Locate every uninfected red blood cell.
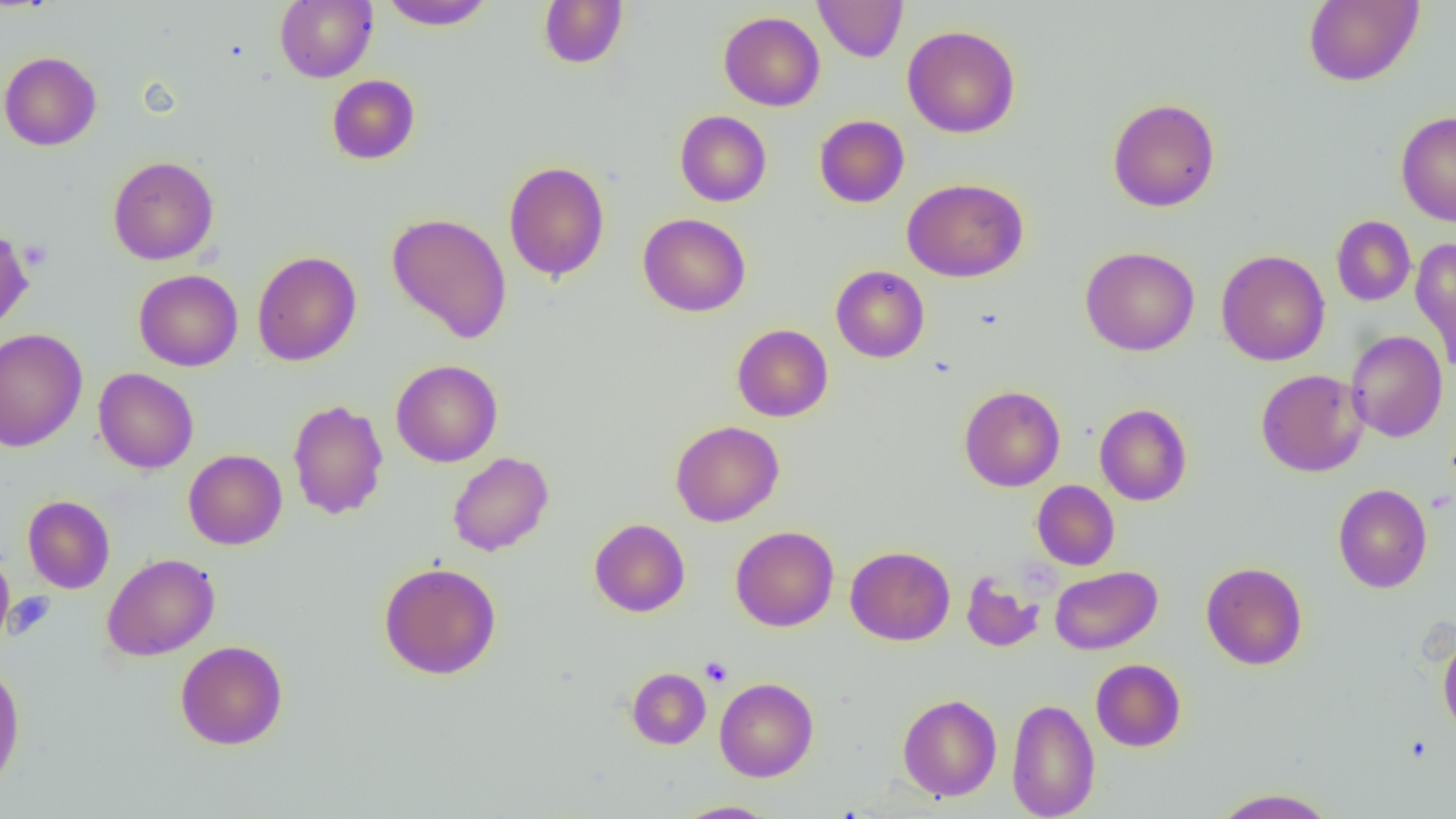

Approximate bounding boxes as [x1, y1, x2, y2] in pixels.
Uninfected red blood cells: [380, 0, 495, 31], [538, 0, 628, 69], [814, 0, 908, 62], [1303, 0, 1424, 87], [275, 1, 378, 82], [718, 11, 825, 111], [902, 25, 1020, 138], [0, 51, 102, 151], [327, 74, 420, 164], [1108, 97, 1220, 212], [675, 110, 772, 207], [1395, 110, 1456, 226], [814, 115, 909, 207], [107, 155, 219, 265], [503, 160, 610, 281], [902, 178, 1028, 282], [387, 212, 512, 344], [638, 213, 751, 317], [1331, 216, 1415, 306], [0, 225, 33, 333], [1410, 236, 1456, 369], [1080, 246, 1199, 356], [1216, 249, 1330, 366], [252, 250, 361, 366], [830, 265, 930, 363], [134, 269, 243, 371], [732, 324, 833, 422], [0, 328, 87, 452], [1345, 330, 1448, 443], [390, 360, 503, 467], [93, 368, 198, 474], [1255, 369, 1368, 477], [959, 385, 1066, 491], [287, 398, 389, 520], [1095, 403, 1192, 506], [670, 420, 784, 527], [183, 449, 287, 550], [447, 451, 554, 556], [1032, 480, 1119, 570], [1333, 483, 1432, 593], [22, 495, 115, 594], [589, 518, 690, 617], [730, 526, 839, 632], [845, 546, 955, 645], [0, 552, 14, 645], [102, 553, 219, 660], [379, 562, 501, 679], [1201, 562, 1308, 670], [1049, 565, 1163, 655], [961, 571, 1045, 653], [1438, 631, 1456, 740], [175, 640, 288, 750], [1091, 658, 1186, 752], [0, 664, 25, 790], [627, 667, 710, 749], [715, 677, 818, 782], [898, 694, 1002, 801], [1006, 698, 1100, 819], [1210, 788, 1338, 818], [673, 800, 778, 818].

{
  "slide_level_diagnosis": "negative for blood parasites",
  "platelet_locations": "approximate bounding boxes as [x1, y1, x2, y2] in pixels: [19, 239, 51, 269], [700, 656, 733, 687]",
  "preparation": "thin blood smear",
  "modality": "optical microscopy",
  "field_of_view": "one of a larger specimen",
  "magnification": "1000x",
  "image_size": "1456×819 pixels"
}